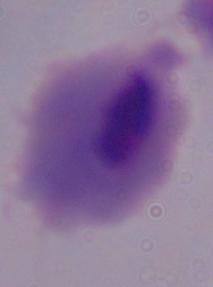
modality = photomicrograph
identification = trichomonad
magnification = 1000x